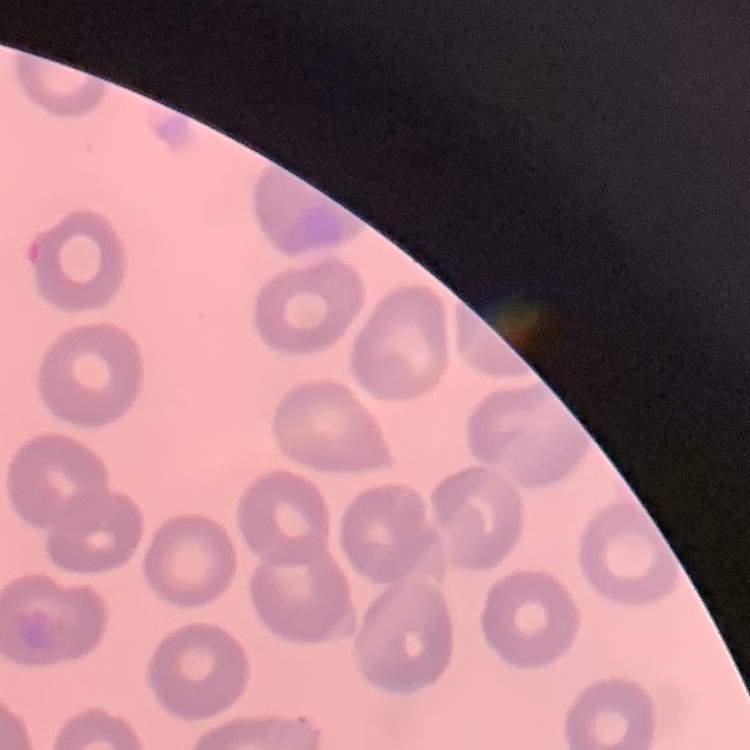

erythrocyte_morphology: no rouleaux formation
image_type: one tile cut from a larger photomicrograph
preparation: thin blood smear
stain: Field's or Giemsa